Classify this cell by malaria status.
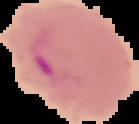

Parasitized.

From a thin blood film. The area outside the segmented cell region is set to black. Image is 139×124 pixels.